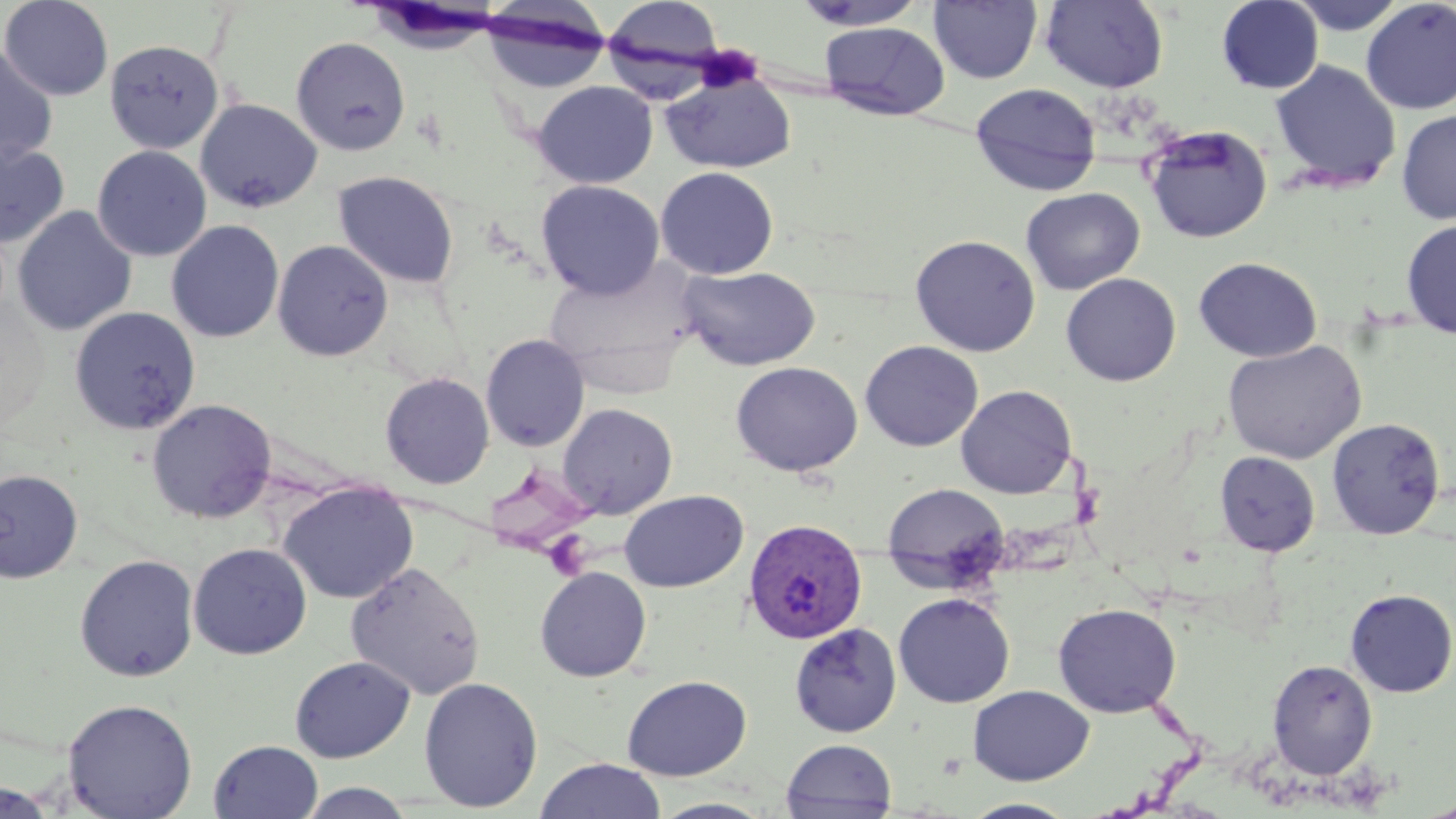
{
  "slide_level_diagnosis": "Plasmodium vivax",
  "stain": "May-Grünwald-Giemsa",
  "uninfected_red_blood_cell_locations": "approximate bounding boxes as (x1,y1)-(x2,y2) corner pairs in pixels: (1,0)-(114,101), (602,0)-(727,79), (792,0)-(929,31), (1287,0)-(1409,35), (929,1)-(1042,84), (1039,1)-(1169,92), (1217,1)-(1324,94), (1360,1)-(1456,114), (478,5)-(613,93), (819,22)-(950,121), (291,36)-(411,155), (104,39)-(225,153), (0,44)-(58,167), (1269,59)-(1402,192), (659,73)-(797,174), (533,81)-(658,188), (969,82)-(1102,196), (195,98)-(322,213), (1396,109)-(1456,225), (1142,124)-(1273,244), (0,141)-(69,248), (92,146)-(211,262), (655,166)-(779,279), (332,171)-(459,289), (536,179)-(664,299), (1020,187)-(1145,295), (11,206)-(137,336), (1400,218)-(1456,339), (166,220)-(284,343), (910,234)-(1041,356), (272,240)-(393,361), (1193,256)-(1322,362), (542,257)-(702,385), (678,266)-(821,370), (1061,272)-(1181,386), (1,297)-(50,432), (69,306)-(201,436), (480,333)-(590,452), (1223,339)-(1366,464), (859,340)-(984,451), (730,360)-(863,477), (380,372)-(495,489), (955,384)-(1077,499), (147,398)-(277,523), (557,403)-(678,519), (1327,416)-(1446,539), (1214,452)-(1320,556), (0,469)-(82,583), (278,481)-(418,603), (881,482)-(1010,586), (619,489)-(748,592), (188,543)-(312,660), (74,554)-(199,682), (345,562)-(486,700), (535,566)-(652,682), (1344,588)-(1456,697), (893,592)-(1015,708), (1053,602)-(1181,718), (789,622)-(901,738), (289,655)-(416,763), (1267,659)-(1378,780), (622,674)-(752,781), (418,675)-(543,812), (968,684)-(1094,785), (61,698)-(198,818), (781,738)-(898,819), (208,740)-(323,819), (534,758)-(667,819), (0,781)-(61,819), (296,782)-(418,818), (649,797)-(777,818), (959,798)-(1079,818), (1415,798)-(1456,819)",
  "modality": "optical microscopy",
  "plasmodium_vivax_infected_red_blood_cell_locations": "approximate bounding boxes as (x1,y1)-(x2,y2) corner pairs in pixels: (743,517)-(868,644)",
  "image_size": "1456×819 pixels",
  "field_of_view": "single",
  "preparation": "thin blood film",
  "magnification": "1000x",
  "platelet_locations": "approximate bounding boxes as (x1,y1)-(x2,y2) corner pairs in pixels: (691,43)-(765,93)"
}